Outline each blood parasite and name the species.
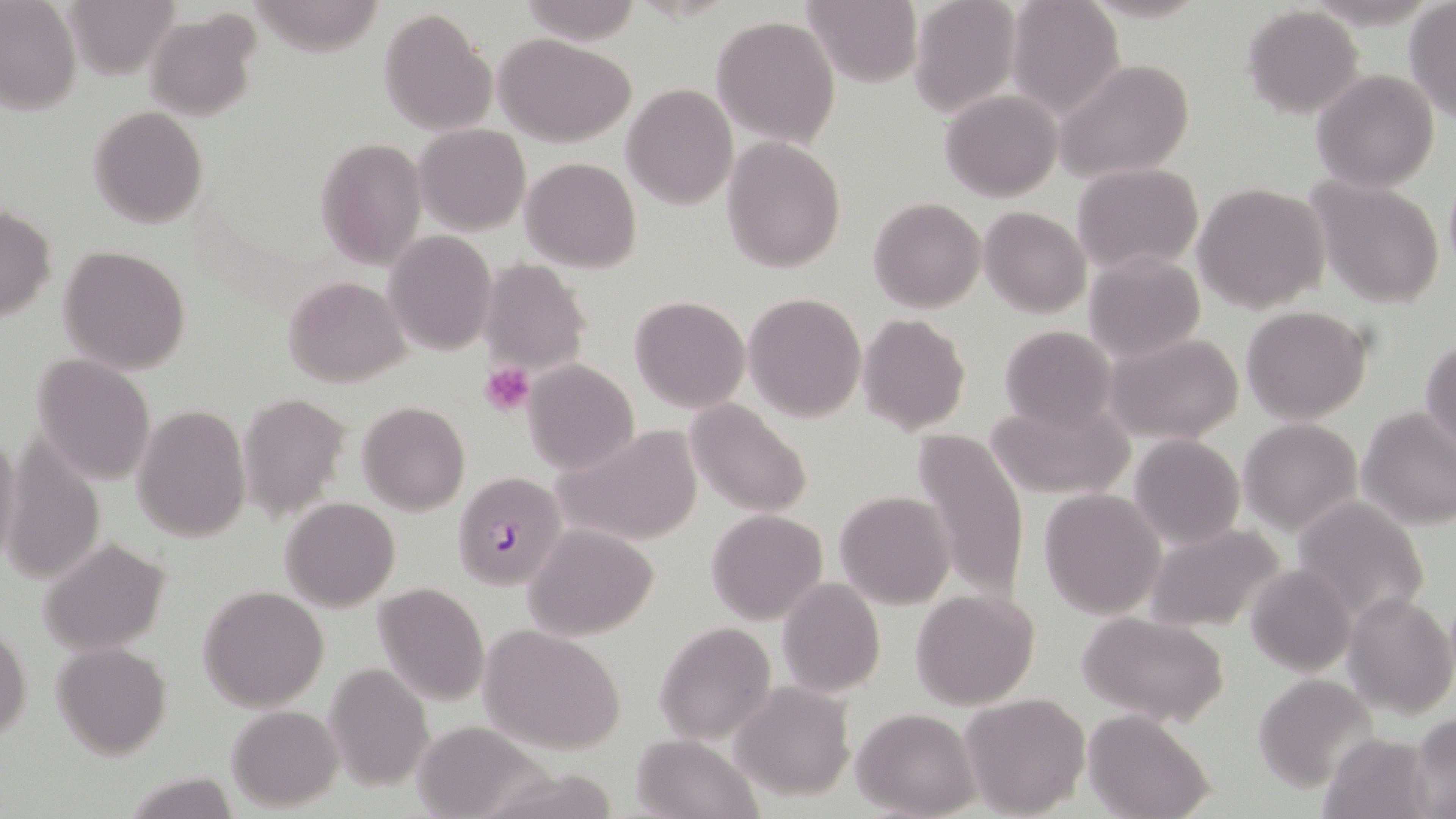
Approximate bounding boxes as (x1, y1, x2, y2) in pixels.
Plasmodium falciparum-infected red blood cells: (452, 470, 569, 591).
No Plasmodium ovale, Plasmodium malariae, Plasmodium vivax, Babesia divergens, or Trypanosoma brucei observed.

slide-level diagnosis = Plasmodium falciparum
platelet locations = approximate bounding boxes as (x1, y1, x2, y2) in pixels: (481, 362, 535, 415)
magnification = 1000x
field of view = one of a larger specimen
preparation = thin blood smear
modality = optical microscopy
image size = 1456×819 pixels
stain = May-Grünwald-Giemsa
uninfected red blood cell locations = approximate bounding boxes as (x1, y1, x2, y2) in pixels: (64, 0, 180, 78), (516, 0, 642, 43), (804, 0, 922, 88), (907, 0, 1021, 117), (0, 1, 82, 116), (1004, 1, 1125, 119), (1404, 3, 1455, 121), (1242, 6, 1365, 118), (380, 7, 497, 137), (145, 10, 260, 121), (711, 15, 841, 146), (1267, 24, 1405, 168), (495, 34, 635, 146), (1051, 59, 1197, 185), (1310, 69, 1439, 191), (622, 83, 738, 209), (941, 90, 1064, 201), (88, 106, 208, 228), (415, 123, 530, 236), (722, 135, 847, 272), (315, 139, 428, 267), (521, 157, 640, 274), (1073, 162, 1204, 273), (1307, 176, 1445, 310), (1193, 182, 1330, 314), (868, 198, 987, 313), (0, 208, 57, 323), (979, 208, 1090, 316), (385, 229, 496, 355), (58, 244, 190, 375), (1084, 251, 1204, 362), (480, 258, 590, 379), (284, 276, 409, 387), (744, 293, 866, 423), (629, 296, 750, 412), (1240, 306, 1373, 426), (859, 314, 971, 436), (1000, 325, 1119, 435), (1106, 331, 1245, 443), (1421, 338, 1455, 460), (31, 354, 156, 485), (523, 359, 638, 474), (239, 392, 350, 521), (987, 396, 1137, 500), (685, 399, 813, 518), (357, 401, 469, 515), (132, 404, 252, 541), (1357, 406, 1456, 529), (1238, 419, 1361, 536), (553, 424, 705, 546), (911, 427, 1031, 603), (0, 428, 24, 569), (1130, 434, 1245, 551), (3, 437, 105, 586), (1039, 488, 1167, 619), (836, 491, 956, 609), (280, 496, 400, 610), (1291, 497, 1431, 627), (707, 509, 828, 626), (1143, 523, 1286, 633), (526, 524, 659, 640), (39, 537, 170, 655), (1246, 564, 1357, 676), (777, 578, 886, 698), (372, 582, 489, 706), (198, 586, 330, 712), (910, 589, 1041, 710), (1342, 592, 1455, 720), (1079, 611, 1230, 727), (654, 620, 777, 746), (1, 625, 32, 744), (482, 625, 625, 755), (53, 643, 170, 759), (323, 661, 432, 789), (1251, 673, 1378, 792), (731, 684, 854, 802), (960, 691, 1090, 818), (228, 705, 342, 810), (852, 706, 981, 817), (1086, 711, 1214, 819), (1410, 712, 1456, 816), (410, 719, 550, 819), (1319, 733, 1436, 818), (632, 734, 762, 819), (122, 770, 238, 819)